Describe the morphology of the red blood cells.
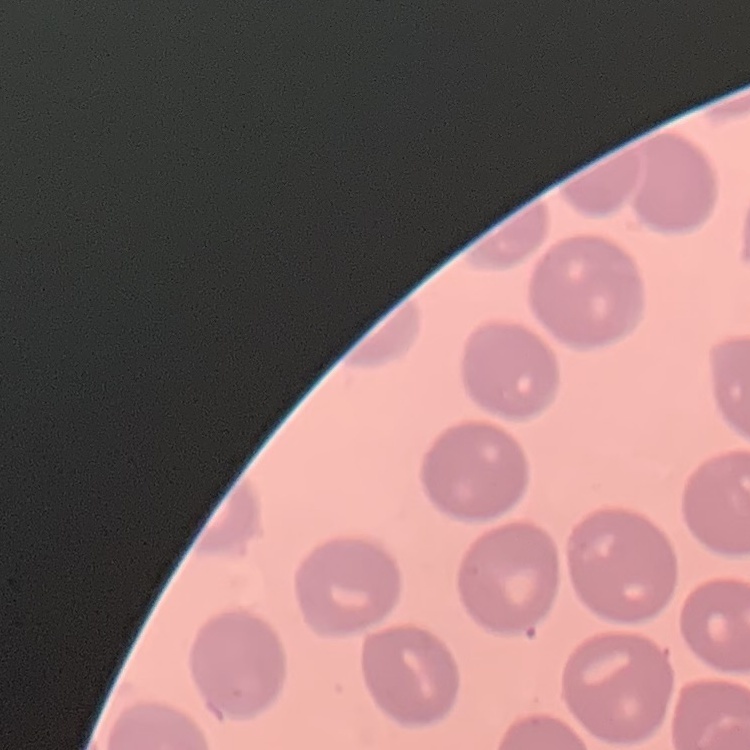
They show no rouleaux formation.

One tile cut from a larger photomicrograph. Field's or Giemsa stain. Thin peripheral smear.